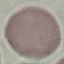
result = no malaria parasites detected
image type = cell patch, automatically extracted from a larger field of view and resized to 64 × 64 pixels
preparation = thin blood film
stain = Giemsa
capture = smartphone camera at the microscope eyepiece